Rate the background quality.
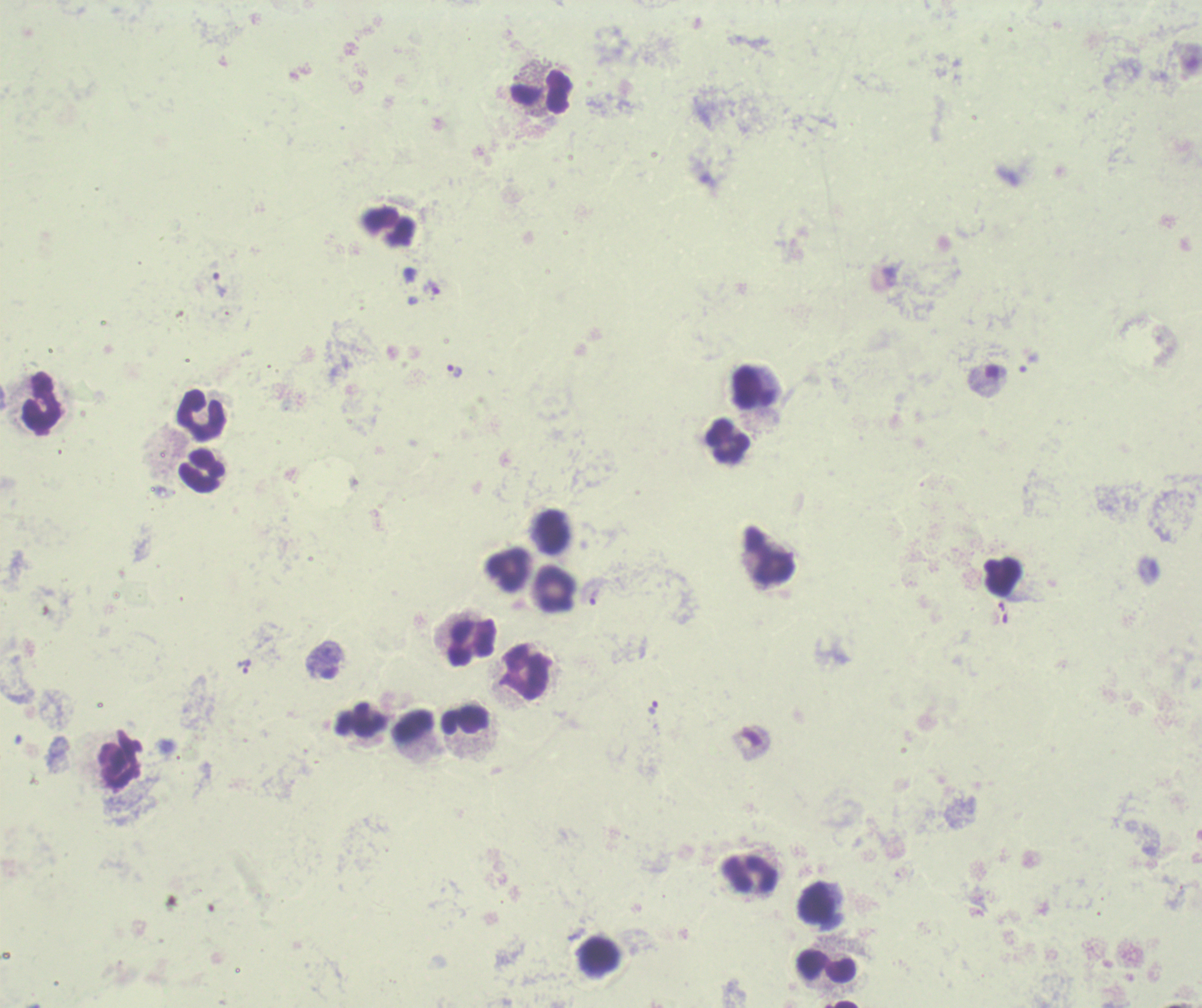
It is poor.

Approximate object centers, in pixels from the top-left corner.
Summary:
  - Trophozoite locations: (x=218, y=278), (x=1030, y=361), (x=455, y=371), (x=595, y=596), (x=243, y=667), (x=653, y=707)
  - Leukocyte locations: (x=540, y=92), (x=388, y=226), (x=752, y=387), (x=42, y=402), (x=201, y=415), (x=727, y=440), (x=202, y=471), (x=551, y=532), (x=769, y=554), (x=508, y=570), (x=555, y=589), (x=472, y=643), (x=526, y=671), (x=465, y=719), (x=361, y=720), (x=415, y=725), (x=119, y=758), (x=750, y=875), (x=817, y=903), (x=600, y=956), (x=826, y=966)
  - Stain: Romanowsky
  - Image size: 1202×1008 pixels
  - Magnification: 100x
  - Context: previously used in a real diagnosis
  - Preparation: thick smear of blood
  - Field of view: single
  - Result: Plasmodium parasites detected